Identify the parasite.
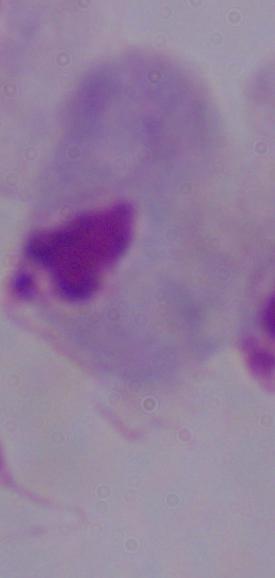

A trichomonad.

magnification: 1000x
modality: micrograph